Name the parasite shown.
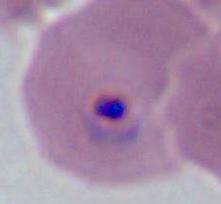
This is Plasmodium.

magnification = 400x or 1000x
modality = photomicrograph